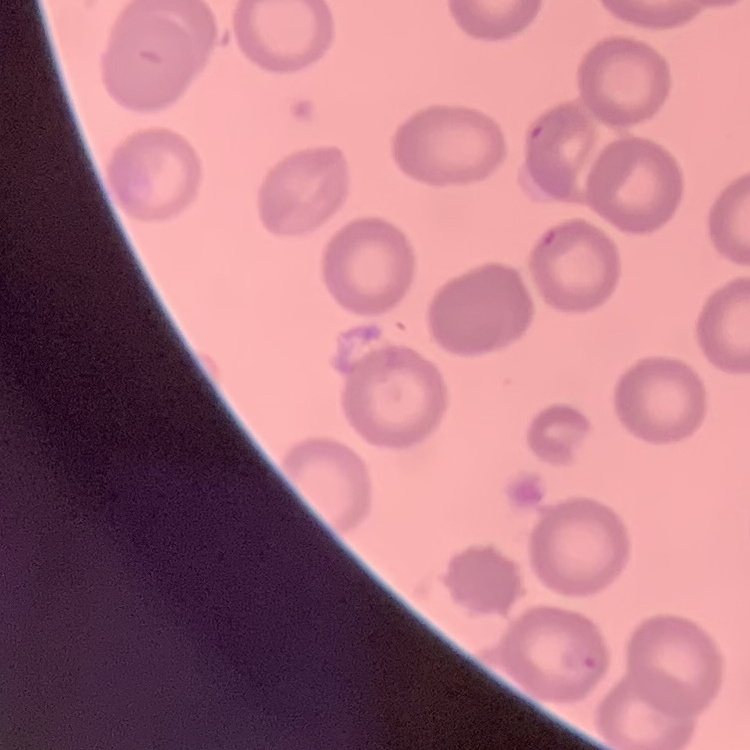

Summary:
  - Red blood cell morphology: no rouleaux formation
  - Stain: Field's or Giemsa
  - Image type: one tile cut from a larger photomicrograph
  - Preparation: thin blood film